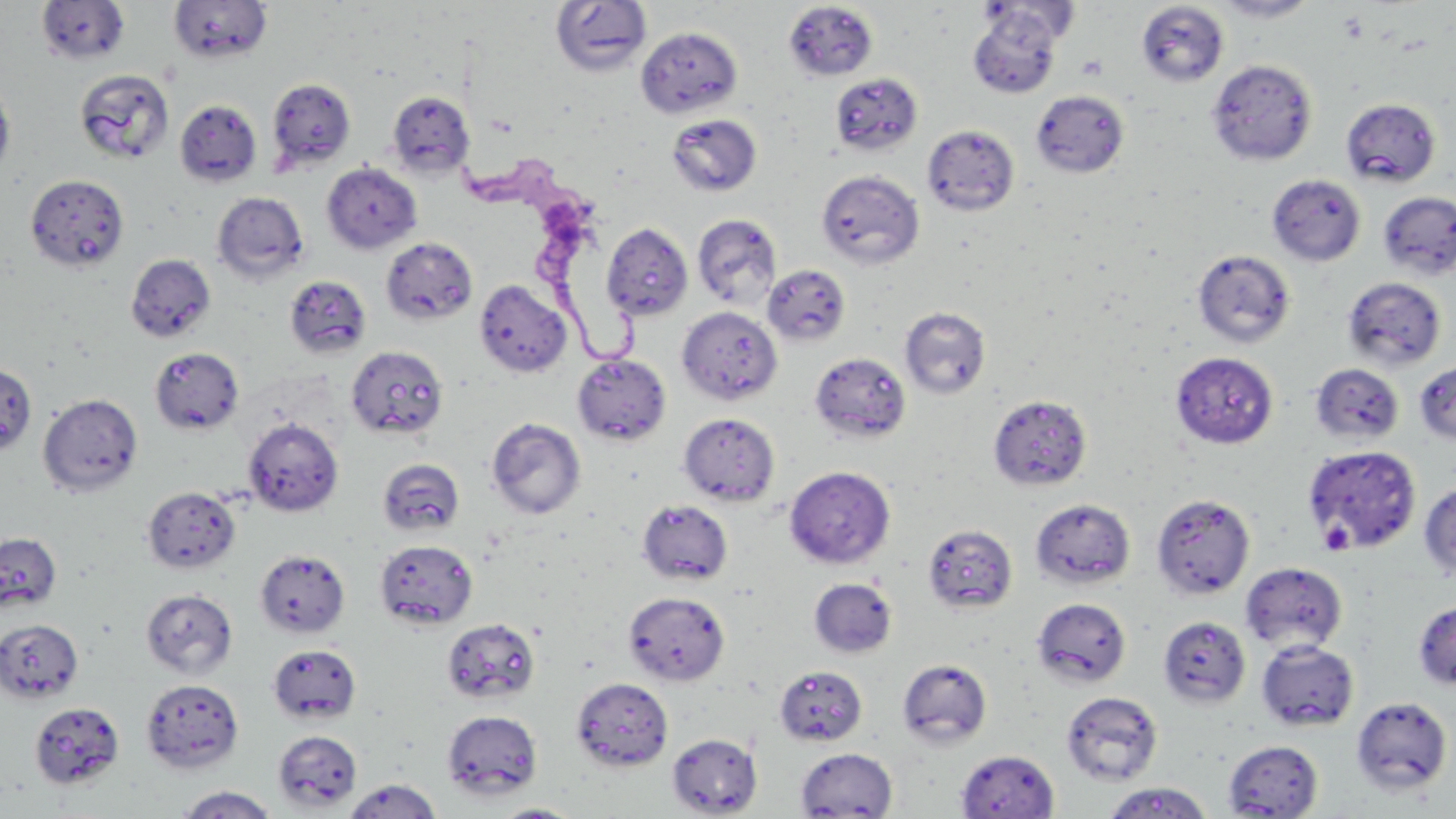
Summary:
  - Coordinate format: approximate bounding boxes as [x1, y1, x2, y2] in pixels
  - Uninfected red blood cell locations: [36, 0, 131, 66], [551, 0, 652, 77], [1210, 0, 1320, 22], [168, 1, 272, 64], [979, 1, 1080, 45], [783, 2, 878, 81], [1135, 2, 1229, 87], [968, 7, 1064, 99], [636, 26, 742, 118], [1206, 59, 1317, 165], [74, 69, 174, 164], [830, 73, 923, 156], [267, 77, 356, 173], [0, 79, 15, 181], [1032, 90, 1129, 178], [386, 91, 473, 178], [1341, 98, 1440, 187], [175, 100, 262, 187], [666, 113, 763, 197], [921, 125, 1020, 216], [321, 162, 422, 254], [816, 170, 924, 269], [26, 174, 129, 272], [1267, 174, 1366, 266], [1377, 190, 1456, 280], [212, 191, 309, 284], [692, 213, 782, 309], [601, 222, 693, 320], [381, 237, 478, 326], [1192, 250, 1296, 348], [125, 254, 215, 342], [763, 264, 851, 346], [284, 275, 371, 359], [1342, 276, 1446, 371], [474, 279, 572, 378], [676, 306, 782, 404], [900, 307, 991, 398], [345, 344, 448, 440], [150, 348, 243, 435], [809, 352, 911, 444], [1171, 352, 1279, 449], [572, 354, 671, 446], [1414, 361, 1456, 445], [0, 363, 37, 457], [1310, 363, 1405, 445], [38, 393, 143, 497], [988, 394, 1092, 490], [679, 412, 779, 506], [243, 417, 343, 516], [486, 417, 586, 519], [1302, 444, 1422, 554], [377, 459, 464, 537], [784, 465, 896, 569], [1419, 482, 1456, 580], [142, 486, 240, 573], [1152, 493, 1256, 600], [637, 499, 734, 586], [1030, 499, 1136, 590], [923, 524, 1018, 614], [0, 533, 61, 612], [374, 539, 478, 630], [254, 549, 350, 638], [1240, 562, 1348, 654], [808, 578, 897, 658], [140, 588, 237, 680], [624, 591, 730, 685], [1032, 597, 1132, 687], [1412, 600, 1456, 689], [1158, 615, 1251, 708], [441, 618, 540, 705], [0, 619, 84, 702], [1257, 639, 1360, 731], [268, 643, 361, 724], [897, 658, 993, 750], [774, 665, 868, 746], [571, 677, 673, 771], [140, 678, 244, 774], [1061, 691, 1164, 785], [1351, 696, 1453, 794], [29, 701, 124, 790], [442, 710, 543, 800], [273, 730, 362, 811], [667, 732, 763, 816], [1223, 740, 1324, 818], [795, 747, 898, 817], [956, 749, 1060, 818], [342, 778, 443, 819], [1103, 782, 1215, 818], [174, 785, 281, 818], [492, 802, 584, 818]
  - Trypanosoma brucei locations: [457, 156, 649, 364]
  - Platelet locations: [1318, 519, 1354, 555]
  - Slide-level diagnosis: Trypanosoma brucei
  - Field of view: single
  - Magnification: 1000x
  - Stain: May-Grünwald-Giemsa
  - Modality: light microscopy
  - Image size: 1456×819 pixels
  - Preparation: thin blood smear